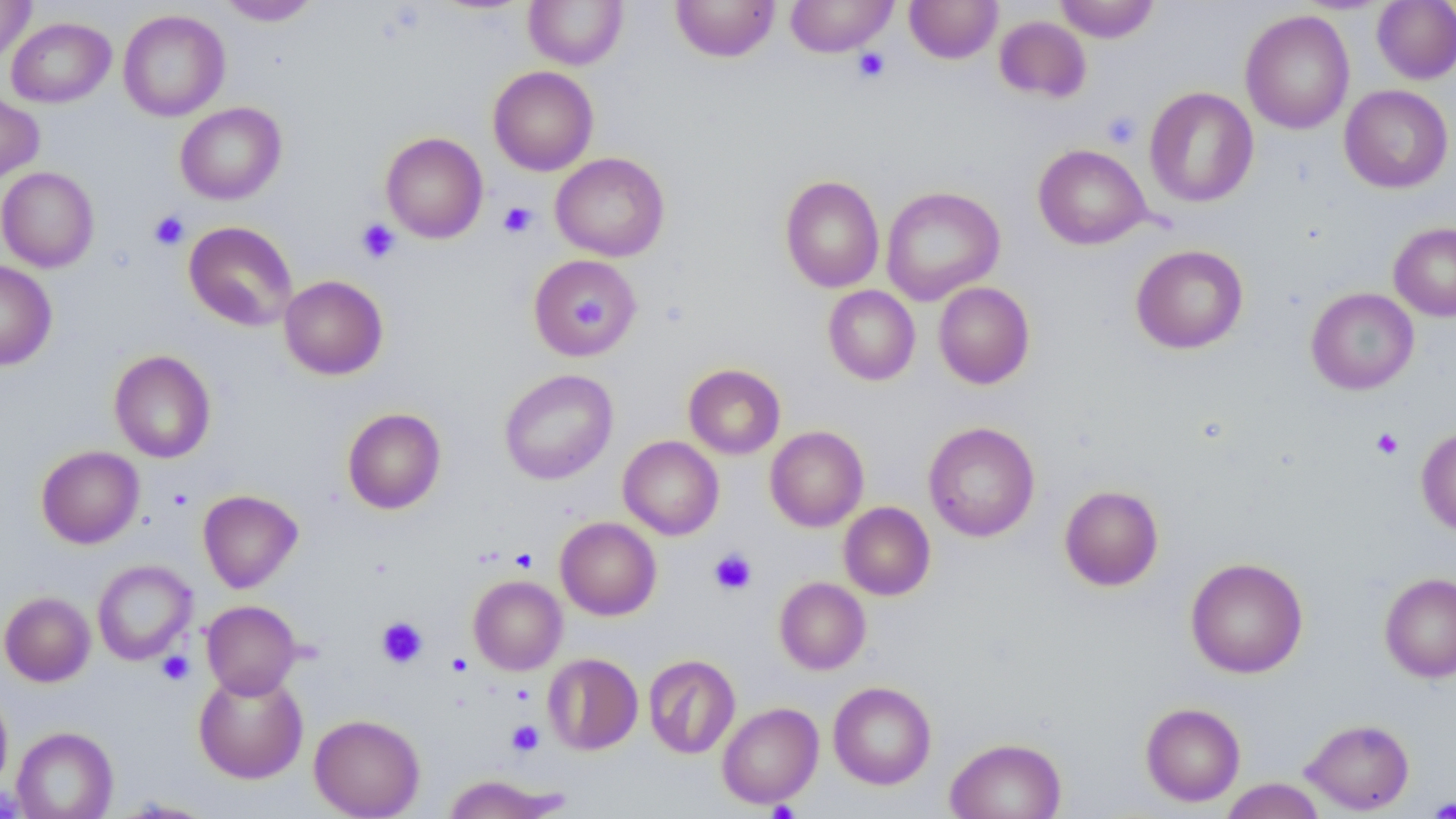
Summary:
  - Coordinate format: approximate bounding boxes as named x1/y1/x2/y2 corners in pixels
  - Platelet locations: (x1=853, y1=47, x2=891, y2=83), (x1=1101, y1=110, x2=1142, y2=149), (x1=498, y1=201, x2=537, y2=238), (x1=149, y1=210, x2=189, y2=250), (x1=356, y1=219, x2=400, y2=263), (x1=571, y1=293, x2=611, y2=334), (x1=1371, y1=428, x2=1403, y2=459), (x1=509, y1=547, x2=537, y2=572), (x1=709, y1=548, x2=756, y2=596), (x1=375, y1=616, x2=428, y2=668), (x1=157, y1=651, x2=194, y2=685), (x1=506, y1=720, x2=544, y2=756), (x1=1428, y1=797, x2=1455, y2=819)
  - Uninfected red blood cell locations: (x1=0, y1=0, x2=35, y2=64), (x1=217, y1=0, x2=321, y2=26), (x1=524, y1=0, x2=628, y2=69), (x1=670, y1=0, x2=780, y2=62), (x1=785, y1=0, x2=898, y2=57), (x1=905, y1=0, x2=1002, y2=63), (x1=1054, y1=0, x2=1160, y2=42), (x1=1372, y1=1, x2=1456, y2=85), (x1=118, y1=9, x2=230, y2=121), (x1=1240, y1=10, x2=1355, y2=135), (x1=994, y1=15, x2=1091, y2=102), (x1=6, y1=17, x2=115, y2=108), (x1=488, y1=66, x2=598, y2=176), (x1=1339, y1=85, x2=1453, y2=194), (x1=1144, y1=87, x2=1259, y2=207), (x1=0, y1=91, x2=44, y2=183), (x1=175, y1=102, x2=287, y2=204), (x1=381, y1=132, x2=488, y2=243), (x1=1033, y1=144, x2=1152, y2=249), (x1=550, y1=152, x2=670, y2=261), (x1=0, y1=167, x2=99, y2=272), (x1=780, y1=175, x2=884, y2=293), (x1=880, y1=186, x2=1005, y2=305), (x1=183, y1=221, x2=298, y2=331), (x1=1389, y1=222, x2=1456, y2=321), (x1=1130, y1=244, x2=1249, y2=354), (x1=528, y1=254, x2=641, y2=359), (x1=0, y1=260, x2=57, y2=370), (x1=279, y1=275, x2=388, y2=380), (x1=933, y1=282, x2=1035, y2=389), (x1=823, y1=285, x2=920, y2=385), (x1=1306, y1=288, x2=1419, y2=394), (x1=109, y1=350, x2=216, y2=463), (x1=683, y1=363, x2=786, y2=459), (x1=499, y1=369, x2=618, y2=485), (x1=342, y1=407, x2=446, y2=514), (x1=923, y1=421, x2=1040, y2=542), (x1=765, y1=426, x2=869, y2=531), (x1=1416, y1=426, x2=1456, y2=537), (x1=618, y1=435, x2=724, y2=540), (x1=36, y1=445, x2=144, y2=548), (x1=1059, y1=484, x2=1164, y2=591), (x1=198, y1=489, x2=303, y2=593), (x1=839, y1=502, x2=935, y2=600), (x1=555, y1=517, x2=661, y2=620), (x1=1185, y1=557, x2=1308, y2=679), (x1=93, y1=560, x2=196, y2=665), (x1=1379, y1=572, x2=1456, y2=682), (x1=469, y1=575, x2=567, y2=675), (x1=775, y1=577, x2=871, y2=674), (x1=0, y1=591, x2=96, y2=686), (x1=201, y1=600, x2=301, y2=698), (x1=543, y1=653, x2=643, y2=755), (x1=643, y1=654, x2=740, y2=759), (x1=193, y1=669, x2=308, y2=783), (x1=828, y1=681, x2=936, y2=790), (x1=0, y1=684, x2=13, y2=797), (x1=717, y1=702, x2=824, y2=809), (x1=1140, y1=702, x2=1245, y2=806), (x1=309, y1=714, x2=425, y2=818), (x1=1300, y1=718, x2=1415, y2=814), (x1=11, y1=726, x2=118, y2=819), (x1=945, y1=737, x2=1066, y2=819), (x1=443, y1=774, x2=560, y2=818), (x1=1220, y1=778, x2=1327, y2=819), (x1=112, y1=798, x2=217, y2=817)
  - Slide-level diagnosis: no evidence of blood parasites
  - Modality: optical microscopy
  - Preparation: thin blood film
  - Image size: 1456×819 pixels
  - Field of view: one of a larger specimen
  - Stain: May-Grünwald-Giemsa
  - Magnification: 1000x